Report the malaria status of this cell.
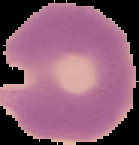

It is parasitized.

Image is 139×145 pixels. The area outside the segmented cell region is set to black. From a thin blood film.